Point out each leukocyte.
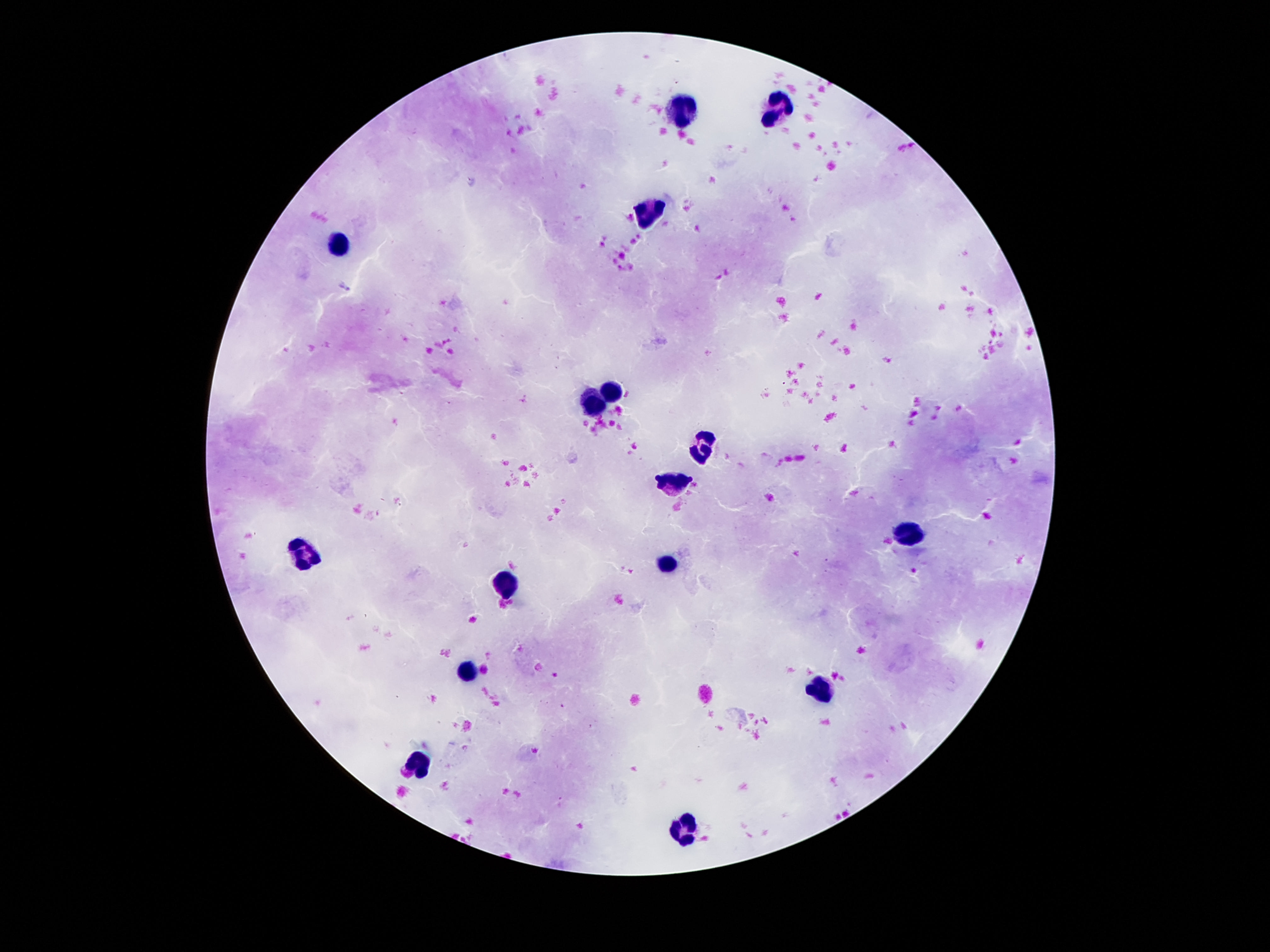

Approximate centers as {x, y} in pixels.
Leukocytes: {680, 110}, {776, 110}, {654, 209}, {338, 244}, {608, 391}, {594, 406}, {702, 442}, {674, 482}, {906, 536}, {300, 555}, {666, 564}, {504, 587}, {468, 676}, {818, 688}, {418, 768}, {684, 828}.

Smartphone photograph taken through the microscope eyepiece. Giemsa stain. Patient malaria status: uninfected. Image is 1270×952 pixels. Thick blood film. 100x magnification. Single field of view.